Locate every uninfected red blood cell.
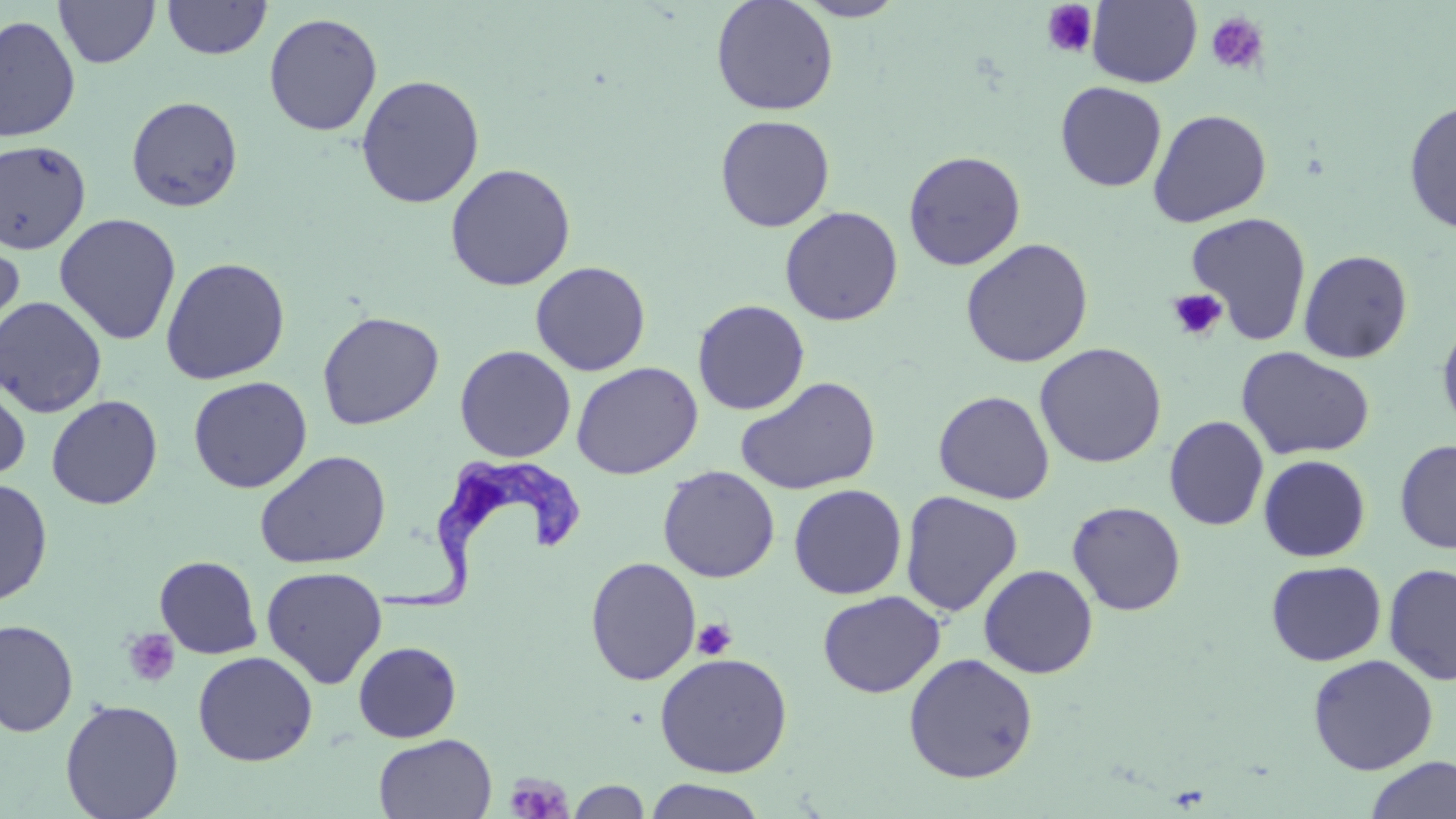
Approximate bounding boxes as named x1/y1/x2/y2 corners in pixels.
Uninfected red blood cells: (x1=54, y1=0, x2=160, y2=68), (x1=162, y1=0, x2=272, y2=60), (x1=710, y1=0, x2=839, y2=116), (x1=795, y1=0, x2=906, y2=21), (x1=1087, y1=0, x2=1201, y2=88), (x1=263, y1=12, x2=383, y2=137), (x1=0, y1=14, x2=81, y2=143), (x1=356, y1=74, x2=485, y2=208), (x1=1055, y1=81, x2=1167, y2=192), (x1=126, y1=95, x2=243, y2=212), (x1=1403, y1=99, x2=1456, y2=235), (x1=1147, y1=108, x2=1272, y2=228), (x1=714, y1=114, x2=835, y2=232), (x1=0, y1=139, x2=91, y2=255), (x1=903, y1=150, x2=1026, y2=271), (x1=445, y1=163, x2=576, y2=291), (x1=779, y1=206, x2=903, y2=326), (x1=1184, y1=212, x2=1313, y2=345), (x1=54, y1=213, x2=181, y2=346), (x1=0, y1=234, x2=25, y2=351), (x1=960, y1=237, x2=1094, y2=368), (x1=1298, y1=249, x2=1413, y2=363), (x1=160, y1=256, x2=290, y2=384), (x1=530, y1=261, x2=651, y2=376), (x1=0, y1=296, x2=107, y2=418), (x1=692, y1=299, x2=809, y2=415), (x1=317, y1=311, x2=444, y2=430), (x1=1436, y1=316, x2=1456, y2=438), (x1=1034, y1=342, x2=1167, y2=468), (x1=454, y1=345, x2=576, y2=463), (x1=1236, y1=346, x2=1375, y2=460), (x1=571, y1=361, x2=703, y2=480), (x1=0, y1=372, x2=31, y2=484), (x1=188, y1=376, x2=312, y2=493), (x1=735, y1=376, x2=881, y2=496), (x1=933, y1=390, x2=1055, y2=504), (x1=46, y1=395, x2=163, y2=509), (x1=1164, y1=416, x2=1269, y2=531), (x1=1395, y1=439, x2=1456, y2=554), (x1=254, y1=449, x2=391, y2=569), (x1=1258, y1=455, x2=1371, y2=562), (x1=658, y1=465, x2=780, y2=583), (x1=0, y1=478, x2=53, y2=605), (x1=788, y1=484, x2=907, y2=599), (x1=900, y1=490, x2=1023, y2=616), (x1=1067, y1=501, x2=1187, y2=616), (x1=154, y1=555, x2=262, y2=659), (x1=585, y1=556, x2=702, y2=686), (x1=1266, y1=560, x2=1386, y2=666), (x1=1383, y1=563, x2=1456, y2=686), (x1=978, y1=564, x2=1098, y2=679), (x1=261, y1=566, x2=387, y2=689), (x1=817, y1=590, x2=945, y2=698), (x1=0, y1=619, x2=79, y2=737), (x1=352, y1=641, x2=462, y2=743), (x1=193, y1=650, x2=318, y2=766), (x1=654, y1=652, x2=793, y2=778), (x1=903, y1=652, x2=1039, y2=783), (x1=1307, y1=653, x2=1438, y2=775), (x1=60, y1=698, x2=184, y2=819), (x1=373, y1=733, x2=496, y2=818), (x1=1364, y1=755, x2=1456, y2=819), (x1=565, y1=778, x2=654, y2=818), (x1=642, y1=779, x2=769, y2=819).

{
  "slide_level_diagnosis": "Trypanosoma brucei",
  "stain": "May-Grünwald-Giemsa",
  "magnification": "1000x",
  "trypanosoma_brucei_locations": "approximate bounding boxes as named x1/y1/x2/y2 corners in pixels: (x1=375, y1=461, x2=584, y2=620)",
  "image_size": "1456×819 pixels",
  "field_of_view": "single",
  "platelet_locations": "approximate bounding boxes as named x1/y1/x2/y2 corners in pixels: (x1=1042, y1=1, x2=1098, y2=59), (x1=1205, y1=11, x2=1270, y2=76), (x1=1166, y1=289, x2=1228, y2=341), (x1=692, y1=618, x2=737, y2=661), (x1=121, y1=628, x2=180, y2=688), (x1=504, y1=772, x2=573, y2=818)",
  "preparation": "thin blood film",
  "modality": "light microscopy"
}